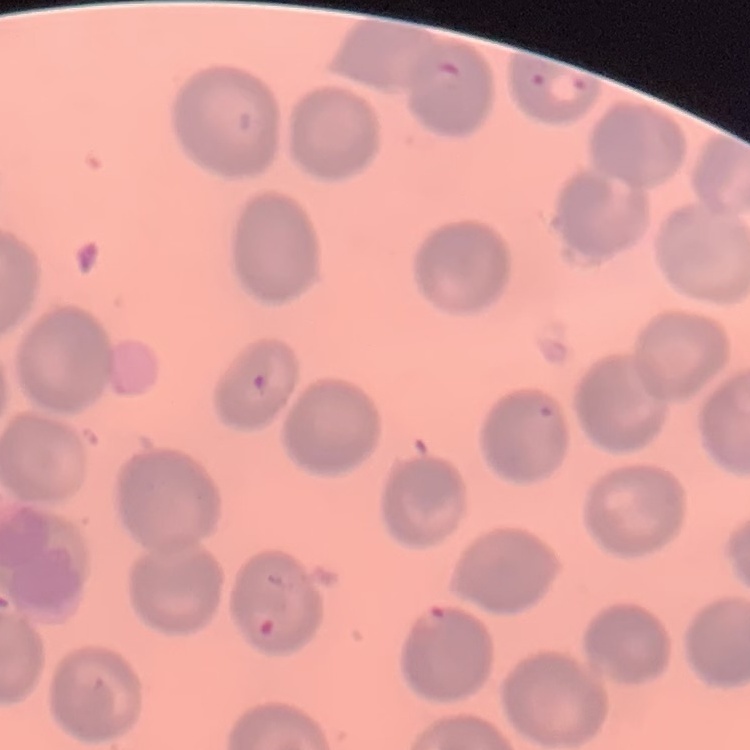

Summary:
  - Red blood cell morphology: no rouleaux formation
  - Image type: square crop of a larger photomicrograph
  - Stain: Field's or Giemsa
  - Preparation: thin blood film